Name the blood parasite species.
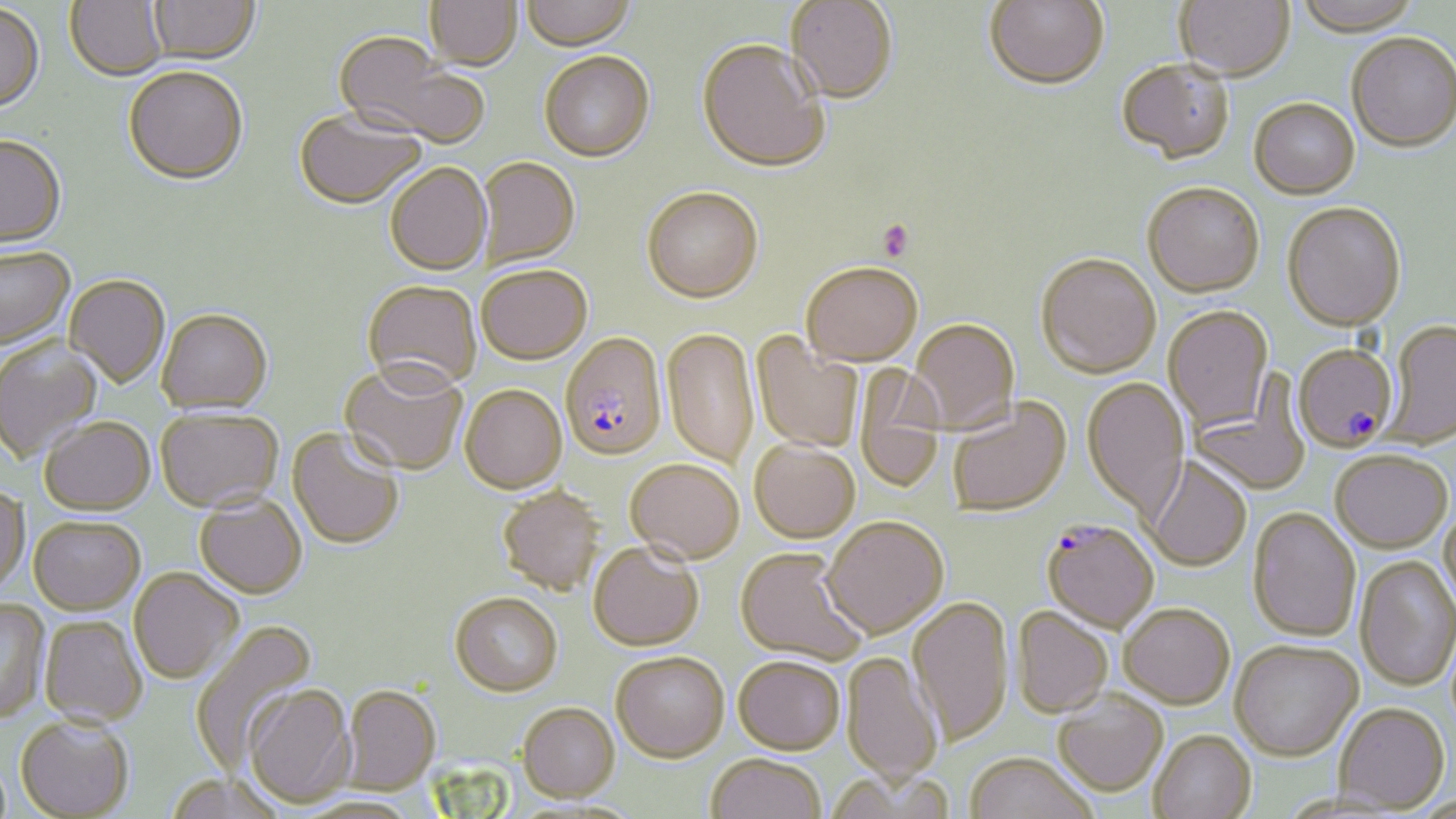

Plasmodium falciparum.

Approximate bounding boxes as (x1,y1)-(x2,y2) corner pairs in pixels. Uninfected red blood cell locations: (64,0)-(167,80), (147,0)-(260,62), (426,0)-(522,69), (522,0)-(635,49), (785,0)-(898,104), (984,0)-(1109,92), (1175,0)-(1294,82), (1291,0)-(1424,38), (0,4)-(46,114), (333,33)-(488,147), (1346,34)-(1456,155), (697,37)-(830,172), (539,50)-(655,160), (1116,61)-(1235,166), (122,65)-(248,183), (1249,100)-(1360,200), (294,107)-(426,208), (0,134)-(66,246), (478,156)-(580,267), (385,162)-(491,274), (1141,181)-(1265,297), (641,185)-(763,301), (1281,201)-(1407,331), (0,245)-(75,347), (1035,252)-(1161,377), (801,260)-(923,364), (477,264)-(591,363), (65,274)-(170,387), (362,279)-(482,390), (1163,306)-(1273,431), (157,307)-(273,413), (909,317)-(1020,432), (1382,320)-(1456,448), (662,327)-(760,470), (752,333)-(864,454), (0,337)-(102,461), (338,358)-(469,475), (854,367)-(946,491), (1190,375)-(1311,497), (1082,377)-(1190,518), (460,383)-(567,492), (947,397)-(1071,517), (155,407)-(283,512), (40,415)-(155,514), (287,427)-(405,550), (749,438)-(859,542), (1330,450)-(1452,552), (1143,456)-(1252,571), (626,457)-(744,562), (0,483)-(29,593), (497,485)-(606,595), (195,494)-(307,598), (1439,504)-(1456,612), (1248,506)-(1361,642), (29,516)-(145,614), (822,516)-(948,637), (589,542)-(704,651), (736,547)-(867,665), (1355,556)-(1456,691), (129,567)-(243,684), (449,591)-(563,695), (908,596)-(1014,744), (0,599)-(49,723), (1118,602)-(1235,707), (1011,606)-(1114,718), (40,615)-(147,726), (188,620)-(317,772), (1229,640)-(1362,760), (611,650)-(729,761), (842,651)-(943,784), (733,655)-(844,754), (242,683)-(357,808), (342,684)-(440,794), (1053,690)-(1168,795), (517,702)-(620,800), (1334,702)-(1449,813), (15,714)-(134,818), (1148,729)-(1257,819), (706,752)-(826,819), (964,752)-(1098,819), (164,771)-(288,819), (295,793)-(423,818). Platelet locations: (876,219)-(914,262). Plasmodium falciparum-infected red blood cell locations: (560,331)-(667,460), (1293,343)-(1398,452), (1042,519)-(1158,632). Single field of view. May-Grünwald-Giemsa stain. Captured at 1000x magnification. Optical microscopy. Thin blood film. Image is 1456×819 pixels.